Report the malaria status of this cell.
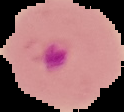

Parasitized.

image type = segmented cell region with the area outside set to black
image size = 124×112 pixels
preparation = thin blood smear